Locate every blood parasite and identify its species.
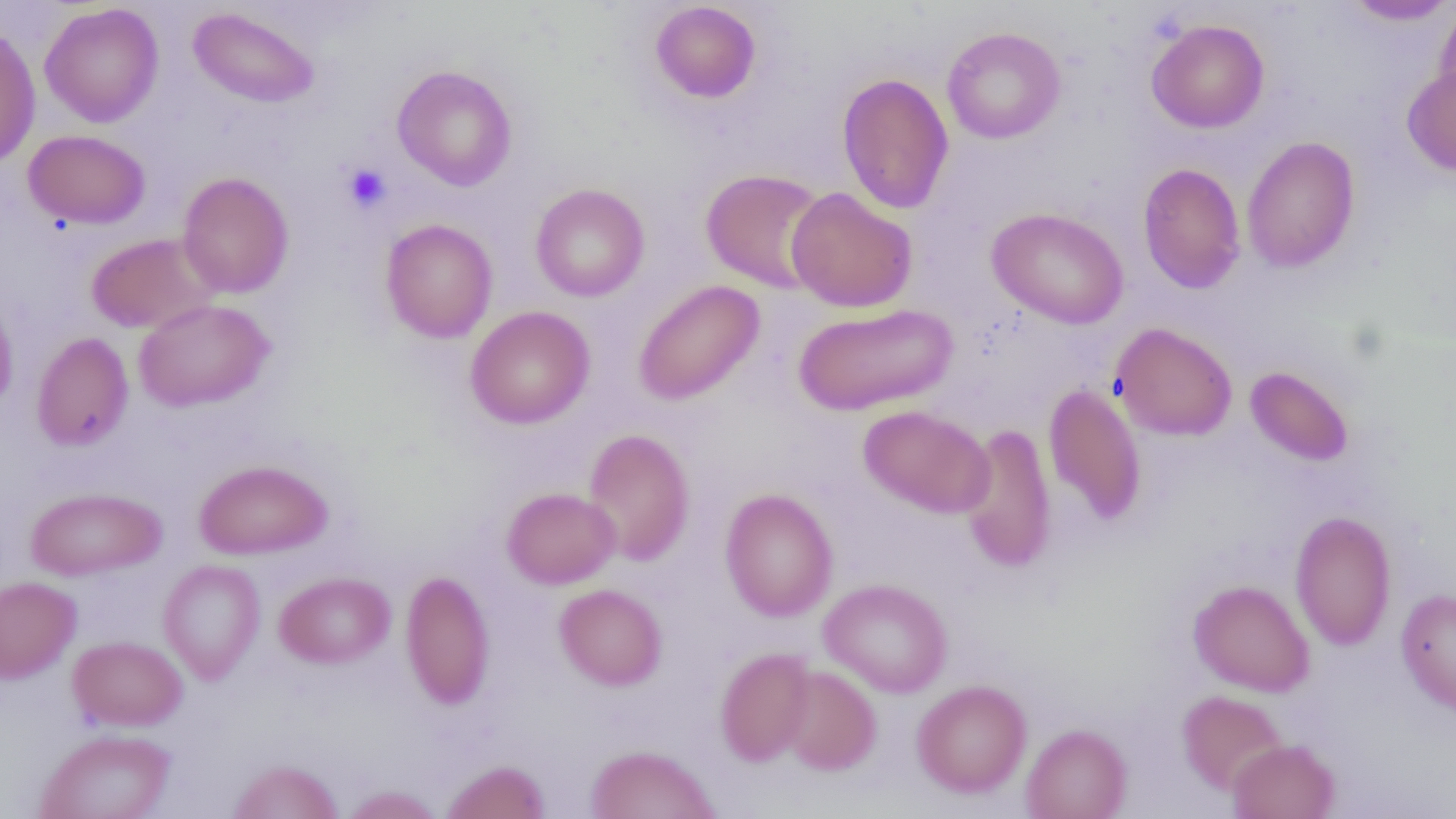

No blood parasites observed.

Approximate bounding boxes as (x1,y1)-(x2,y2) corner pairs in pixels. Platelet locations: (342,163)-(391,214). Uninfected red blood cell locations: (1341,1)-(1456,25), (39,2)-(164,128), (649,2)-(761,104), (1433,2)-(1456,112), (188,6)-(321,108), (1147,19)-(1270,133), (0,24)-(41,168), (941,26)-(1066,144), (392,64)-(518,191), (1402,64)-(1456,177), (836,72)-(954,214), (23,129)-(151,229), (1242,136)-(1360,273), (1137,162)-(1247,295), (701,168)-(829,293), (177,171)-(294,299), (530,183)-(650,302), (786,187)-(917,313), (986,207)-(1129,329), (381,218)-(498,343), (85,232)-(220,334), (633,280)-(765,405), (0,288)-(19,417), (133,299)-(275,412), (793,303)-(958,416), (465,306)-(595,429), (1111,322)-(1237,441), (31,331)-(134,452), (1245,366)-(1354,467), (1043,383)-(1148,527), (858,405)-(994,518), (959,422)-(1057,574), (583,428)-(695,566), (193,459)-(333,559), (25,487)-(167,581), (502,487)-(620,589), (720,488)-(838,622), (1290,510)-(1396,650), (157,559)-(266,684), (401,570)-(495,710), (274,571)-(395,668), (0,576)-(81,683), (818,578)-(953,698), (1189,580)-(1315,696), (554,583)-(667,690), (1396,588)-(1456,715), (68,636)-(188,731), (715,647)-(817,767), (779,665)-(881,776), (911,680)-(1032,798), (1177,690)-(1288,795), (1021,723)-(1132,819), (34,728)-(176,819), (1227,739)-(1340,819), (584,744)-(722,818), (227,758)-(344,819), (441,759)-(551,819), (339,785)-(445,819). Slide-level diagnosis: no evidence of blood parasites. Optical microscopy. Thin blood smear. One field of a larger specimen. 1000x magnification. Image is 1456×819 pixels.